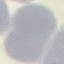
malaria status = uninfected
capture = smartphone through the microscope eyepiece
image type = automatically extracted cell patch, resized to 64 × 64 pixels
stain = Giemsa
preparation = thin blood film